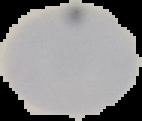

Summary:
  - Image type: cell region segmented out of the field of view; surrounding area masked to black
  - Image size: 142×121 pixels
  - Malaria status: uninfected
  - Preparation: thin blood film